Report the malaria status of this cell.
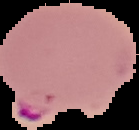

Parasitized.

image_type: segmented cell region with the area outside set to black
preparation: thin blood smear
image_size: 139×130 pixels